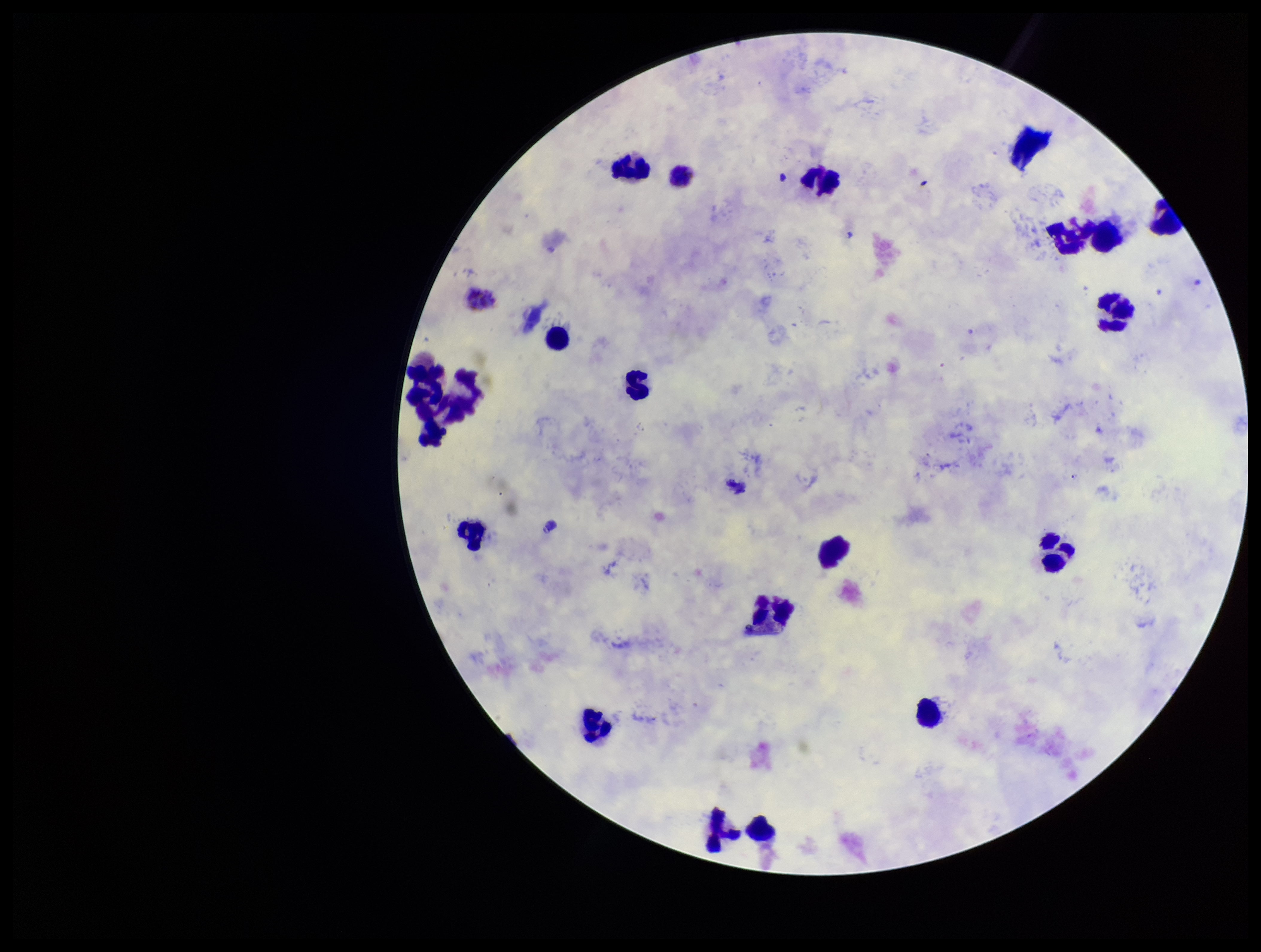
Patient malaria status: positive. Parasite count: 0. Leukocyte count: 22. Single field of view. Plasmodium parasites: none seen. Species reported for this patient: Plasmodium vivax. Smartphone photograph taken through the eyepiece of a microscope. Preparation: thick. Stained with Giemsa. Image is 1261×952 pixels.